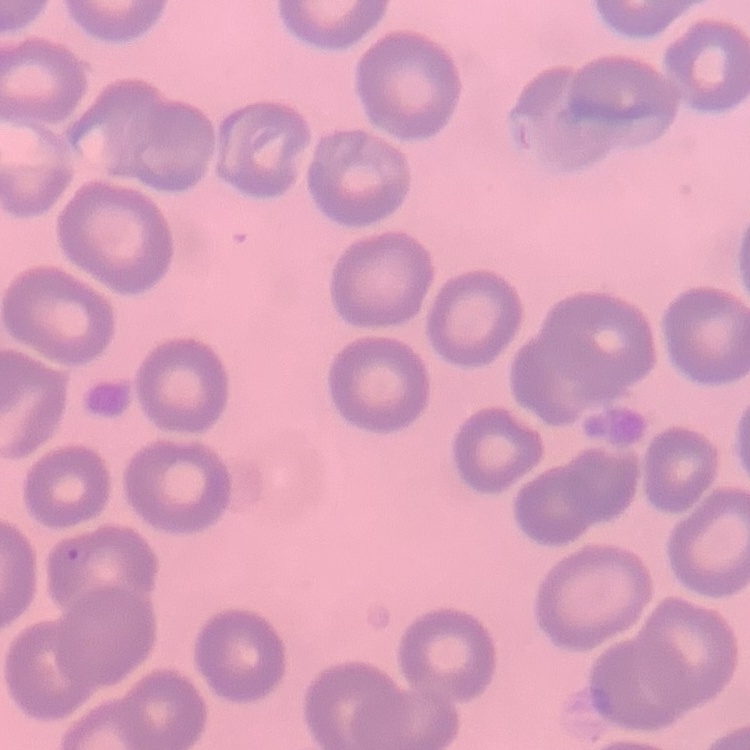
{
  "red_blood_cell_morphology": "no rouleaux formation",
  "stain": "Field's or Giemsa",
  "preparation": "thin peripheral smear",
  "image_type": "square crop of a larger photomicrograph"
}